Locate every uninfected red blood cell.
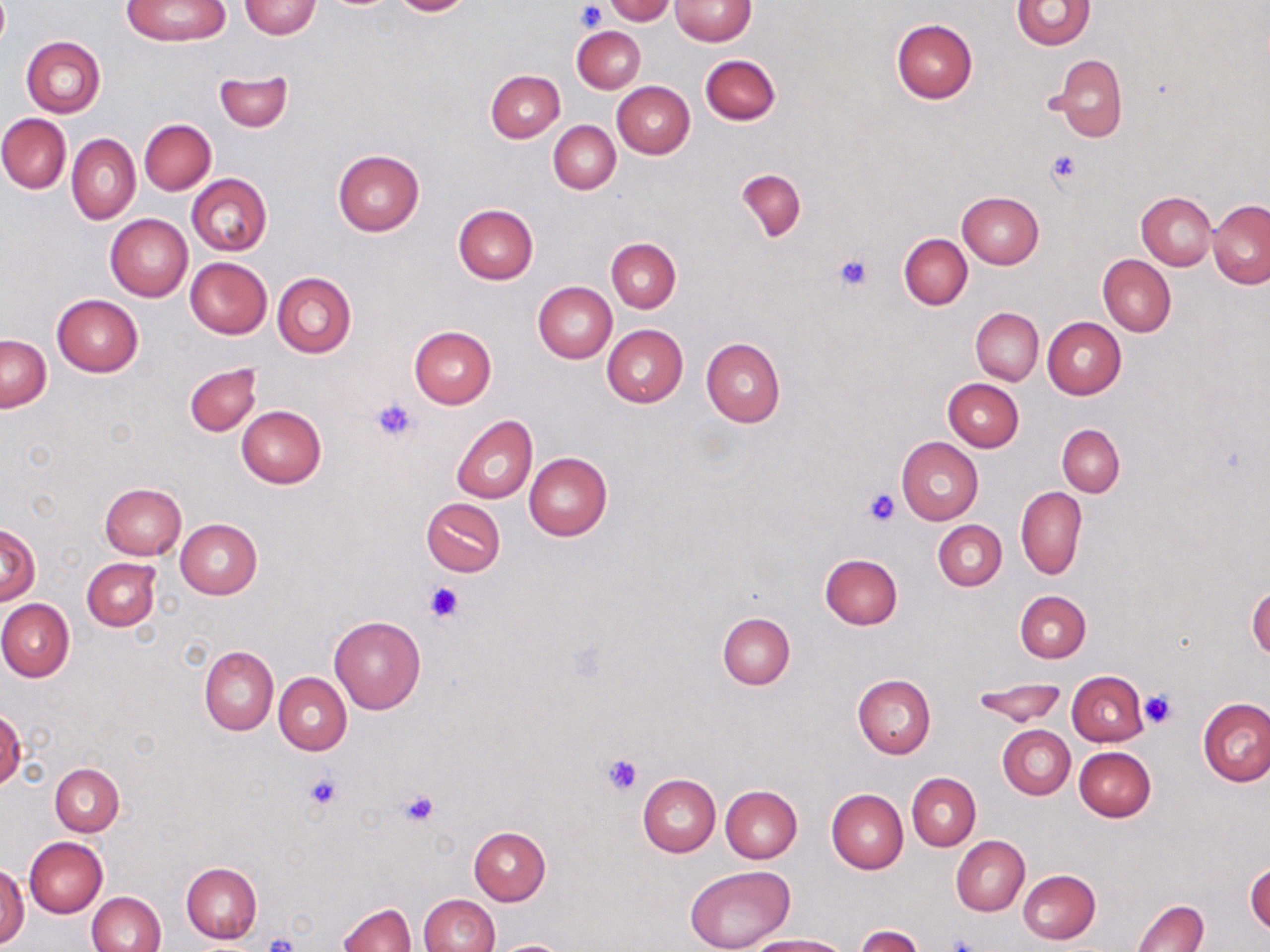

Approximate bounding boxes as [x1, y1, x2, y2] in pixels.
Uninfected red blood cells: [123, 0, 228, 46], [391, 0, 475, 16], [606, 0, 674, 24], [669, 0, 755, 46], [239, 1, 321, 38], [1011, 1, 1097, 50], [891, 19, 978, 103], [573, 26, 645, 92], [21, 36, 105, 117], [1047, 53, 1127, 143], [700, 54, 780, 125], [487, 70, 565, 143], [213, 71, 292, 132], [613, 82, 694, 158], [0, 113, 71, 193], [140, 119, 216, 194], [549, 120, 620, 194], [67, 134, 140, 223], [333, 149, 425, 236], [736, 170, 805, 241], [187, 174, 272, 256], [957, 191, 1045, 269], [1137, 192, 1218, 270], [1208, 201, 1270, 289], [454, 205, 537, 283], [105, 214, 192, 302], [899, 234, 972, 309], [607, 238, 680, 312], [1098, 255, 1176, 336], [185, 257, 271, 337], [185, 265, 351, 344], [272, 272, 356, 358], [534, 281, 617, 363], [52, 295, 142, 377], [971, 308, 1044, 384], [1043, 317, 1125, 399], [602, 325, 688, 407], [408, 327, 496, 409], [1, 335, 51, 411], [701, 338, 785, 426], [185, 363, 261, 437], [942, 379, 1023, 451], [236, 406, 327, 489], [452, 416, 537, 503], [1057, 424, 1124, 496], [897, 436, 983, 524], [525, 453, 612, 540], [100, 483, 187, 559], [1016, 487, 1087, 579], [422, 499, 506, 576], [934, 519, 1007, 590], [176, 521, 262, 598], [1, 526, 39, 603], [820, 554, 902, 628], [82, 558, 160, 630], [1247, 585, 1270, 658], [1014, 590, 1091, 662], [0, 600, 74, 681], [718, 613, 795, 690], [329, 616, 425, 714], [200, 647, 278, 735], [1067, 671, 1147, 746], [274, 673, 352, 755], [853, 675, 935, 759], [970, 681, 1067, 727], [1199, 699, 1270, 786], [0, 708, 25, 791], [998, 725, 1075, 799], [1074, 746, 1156, 821], [50, 762, 124, 837], [908, 774, 980, 851], [637, 775, 719, 856], [720, 785, 802, 863], [826, 788, 908, 873], [469, 827, 550, 904], [951, 836, 1029, 916], [26, 837, 107, 917], [1245, 859, 1269, 934], [181, 862, 262, 942], [0, 865, 29, 946], [686, 866, 796, 952], [1018, 870, 1099, 944], [86, 892, 165, 952], [418, 894, 499, 952], [1133, 898, 1207, 952], [338, 903, 415, 952], [856, 926, 924, 952], [745, 935, 851, 952], [491, 939, 575, 952].

Summary:
  - Platelet locations: [577, 2, 606, 32], [1045, 148, 1083, 185], [833, 254, 874, 294], [370, 397, 420, 446], [865, 489, 898, 525], [425, 580, 463, 621], [1139, 690, 1177, 729], [603, 753, 644, 794], [305, 775, 341, 811], [399, 790, 438, 827], [264, 932, 301, 952]
  - Slide-level diagnosis: no evidence of blood parasites
  - Image size: 1270×952 pixels
  - Modality: light microscopy
  - Stain: May-Grünwald-Giemsa
  - Field of view: one of a larger specimen
  - Magnification: 1000x
  - Preparation: thin blood smear